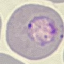 Malaria status: parasitized. Thin smear of blood. Giemsa stain. Cell patch, automatically extracted from a larger field of view and resized to 64 × 64 pixels. Acquired by smartphone through the microscope eyepiece.